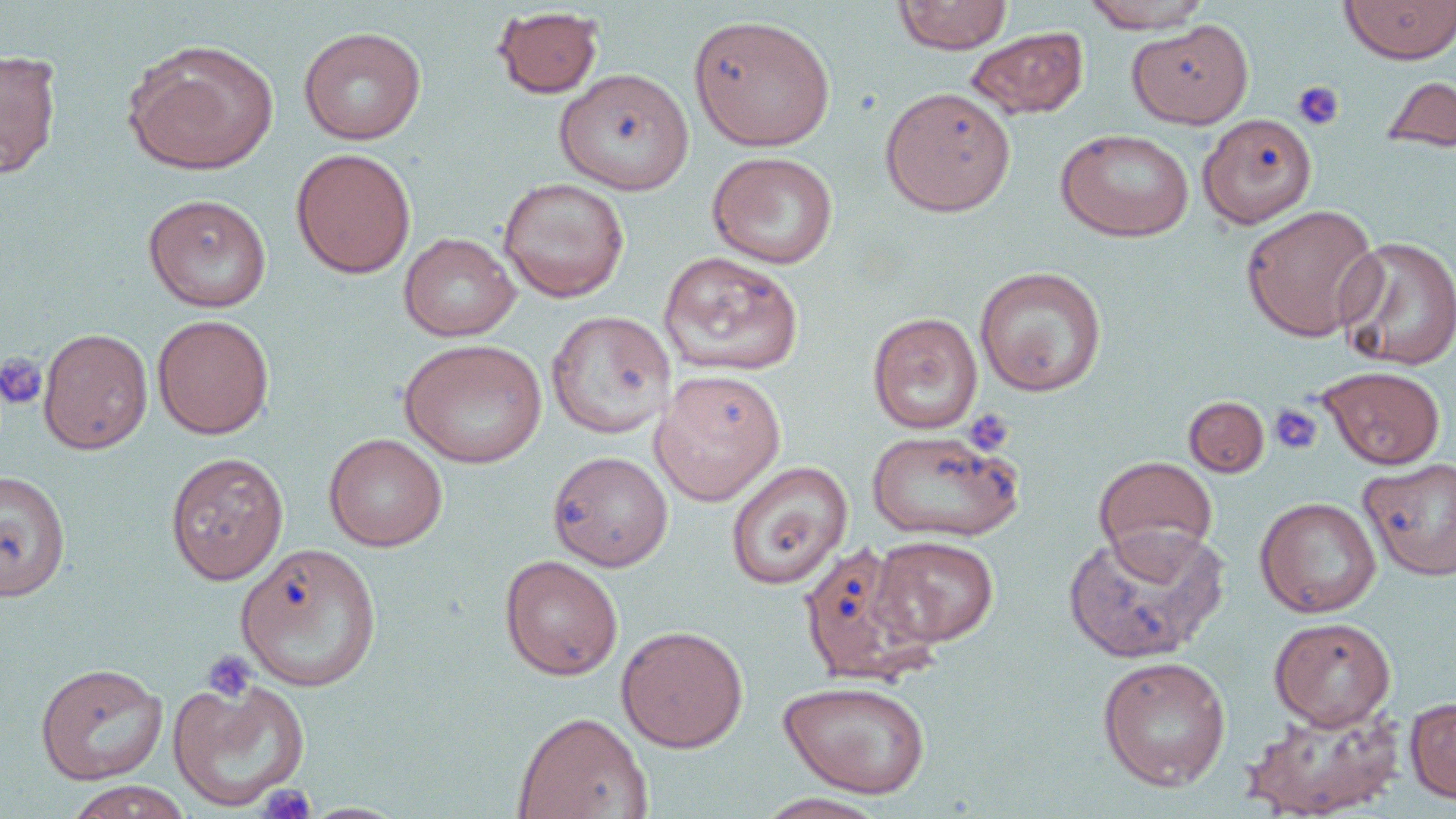
slide_level_diagnosis: no evidence of blood parasites
uninfected_red_blood_cell_locations: 'approximate bounding boxes as [x1, y1, x2, y2] in pixels: [893, 0, 1013, 54], [1339, 0, 1456, 64], [1080, 1, 1214, 32], [491, 6, 604, 99], [688, 13, 836, 151], [1127, 20, 1254, 130], [298, 26, 427, 145], [965, 26, 1088, 119], [124, 39, 278, 176], [0, 48, 62, 179], [554, 69, 694, 194], [1381, 75, 1456, 154], [880, 86, 1016, 217], [1198, 113, 1318, 228], [1056, 128, 1195, 242], [290, 147, 416, 278], [706, 151, 839, 269], [498, 177, 629, 303], [143, 193, 272, 312], [1240, 204, 1382, 342], [398, 232, 520, 342], [1335, 235, 1456, 371], [658, 251, 804, 377], [973, 264, 1108, 397], [546, 311, 677, 439], [867, 312, 983, 434], [151, 314, 274, 439], [38, 327, 153, 454], [398, 339, 548, 468], [1317, 365, 1445, 469], [650, 370, 786, 506], [1184, 396, 1269, 477], [865, 429, 1023, 542], [323, 433, 448, 552], [547, 450, 674, 571], [165, 451, 289, 585], [1093, 455, 1218, 567], [1359, 456, 1456, 581], [725, 461, 852, 590], [0, 469, 71, 601], [1254, 496, 1381, 618], [1062, 527, 1226, 664], [872, 535, 999, 647], [236, 542, 383, 692], [797, 542, 937, 686], [499, 553, 623, 680], [1269, 616, 1395, 730], [616, 625, 749, 752], [1096, 655, 1232, 791], [35, 662, 168, 785], [167, 677, 311, 811], [778, 679, 932, 799], [1404, 697, 1456, 804], [1240, 702, 1406, 818], [512, 711, 652, 819], [63, 780, 195, 819], [753, 793, 892, 819]'
modality: light microscopy
image_size: 1456×819 pixels
preparation: thin blood smear
stain: May-Grünwald-Giemsa
magnification: 1000x
platelet_locations: 'approximate bounding boxes as [x1, y1, x2, y2] in pixels: [1291, 80, 1345, 131], [0, 352, 47, 409], [1269, 403, 1323, 455], [962, 408, 1015, 456], [202, 649, 258, 703], [258, 784, 317, 819]'
field_of_view: single